Give the position of every malaria parasite.
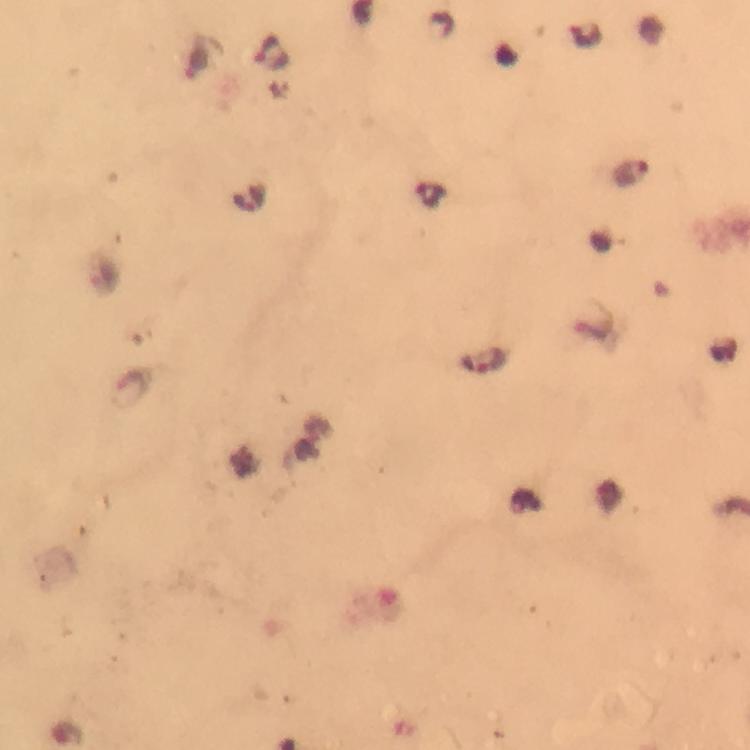
Approximate centers as (x, y) in pixels.
Malaria parasites: (272, 51), (198, 62), (629, 174), (429, 194), (250, 198), (483, 360).

Summary:
  - Magnification: 100x
  - Immersion oil: used
  - Preparation: thick blood smear
  - Stain: Giemsa
  - Context: from a malaria diagnostic workup
  - Cropped from: a single field of view
  - Image size: 750×750 pixels
  - Capture: smartphone camera through the microscope